Describe the morphology of the erythrocytes.
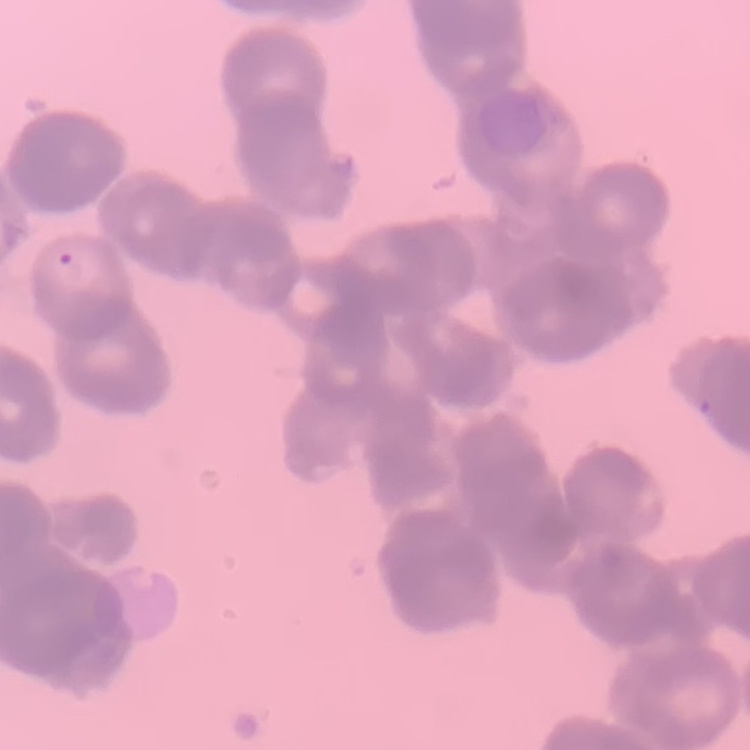
Rouleaux formation.

Field's or Giemsa stain. Square crop of a larger photomicrograph. Thin blood film.